Classify this cell by malaria status.
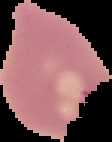

It is uninfected.

{
  "preparation": "thin blood smear",
  "image_type": "segmented cell region with the area outside set to black",
  "image_size": "112×142 pixels"
}